Name the parasite shown.
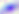
This is Toxoplasma gondii.

Photomicrograph. 400x magnification.